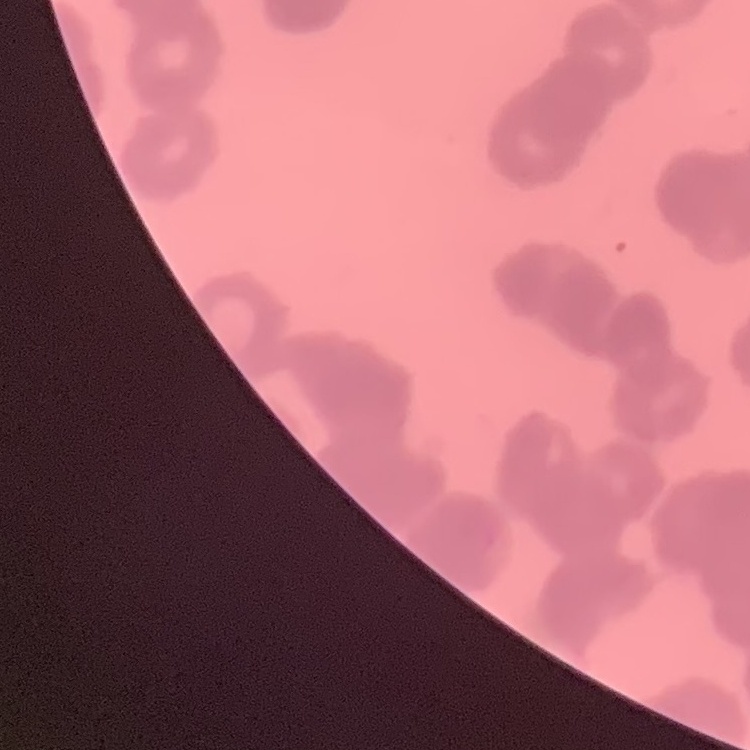

The erythrocytes exhibit rouleaux formation. Thin peripheral smear. Stained with either Field's or Giemsa. One tile cut from a larger photomicrograph.